Assess the morphology of the erythrocytes.
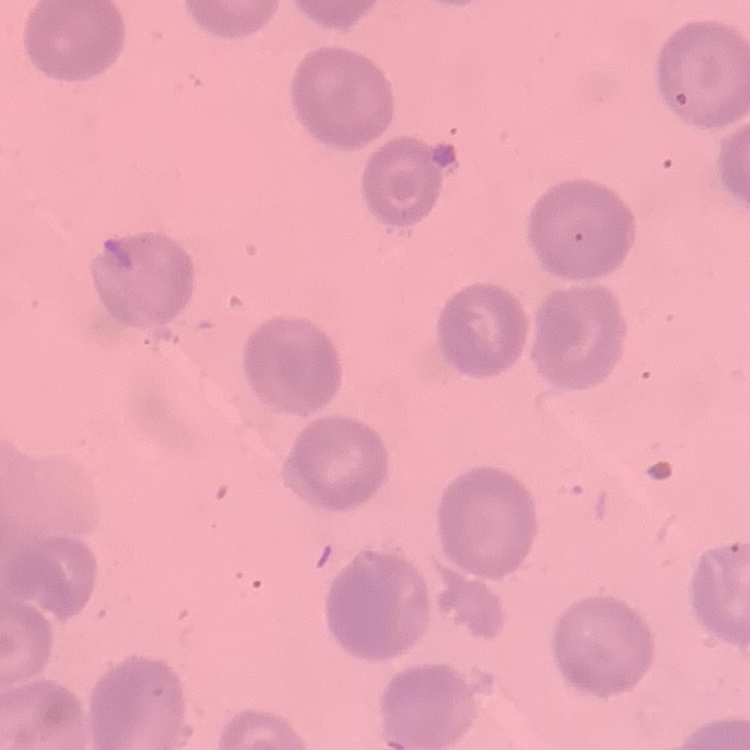
No rouleaux formation.

Square crop of a larger photomicrograph. Thin blood film. Stained with either Field's or Giemsa.